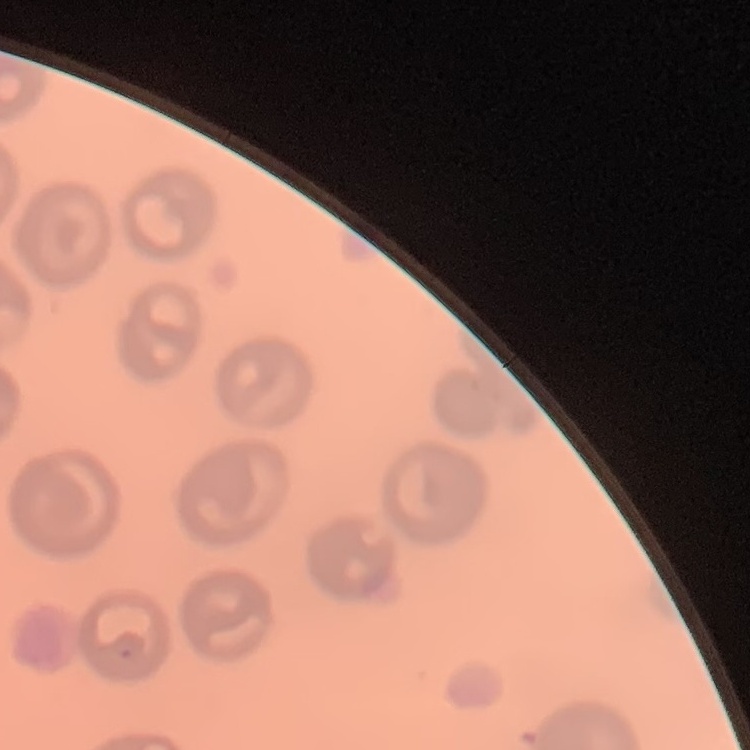
The erythrocytes show no rouleaux formation. Thin peripheral smear. Field's or Giemsa stain. One tile cut from a larger photomicrograph.